Report the malaria status of this cell.
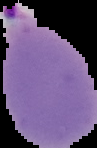
Parasitized.

image type = segmented cell region with the area outside set to black
preparation = thin blood smear
image size = 97×148 pixels